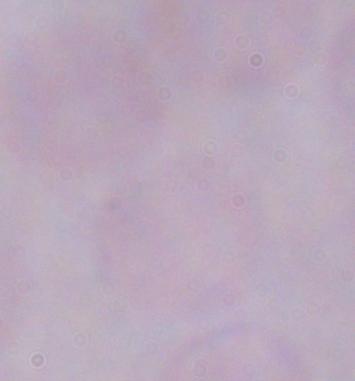
Summary:
  - Magnification: 1000x
  - Identification: trypanosome
  - Modality: micrograph